Name the blood parasite species.
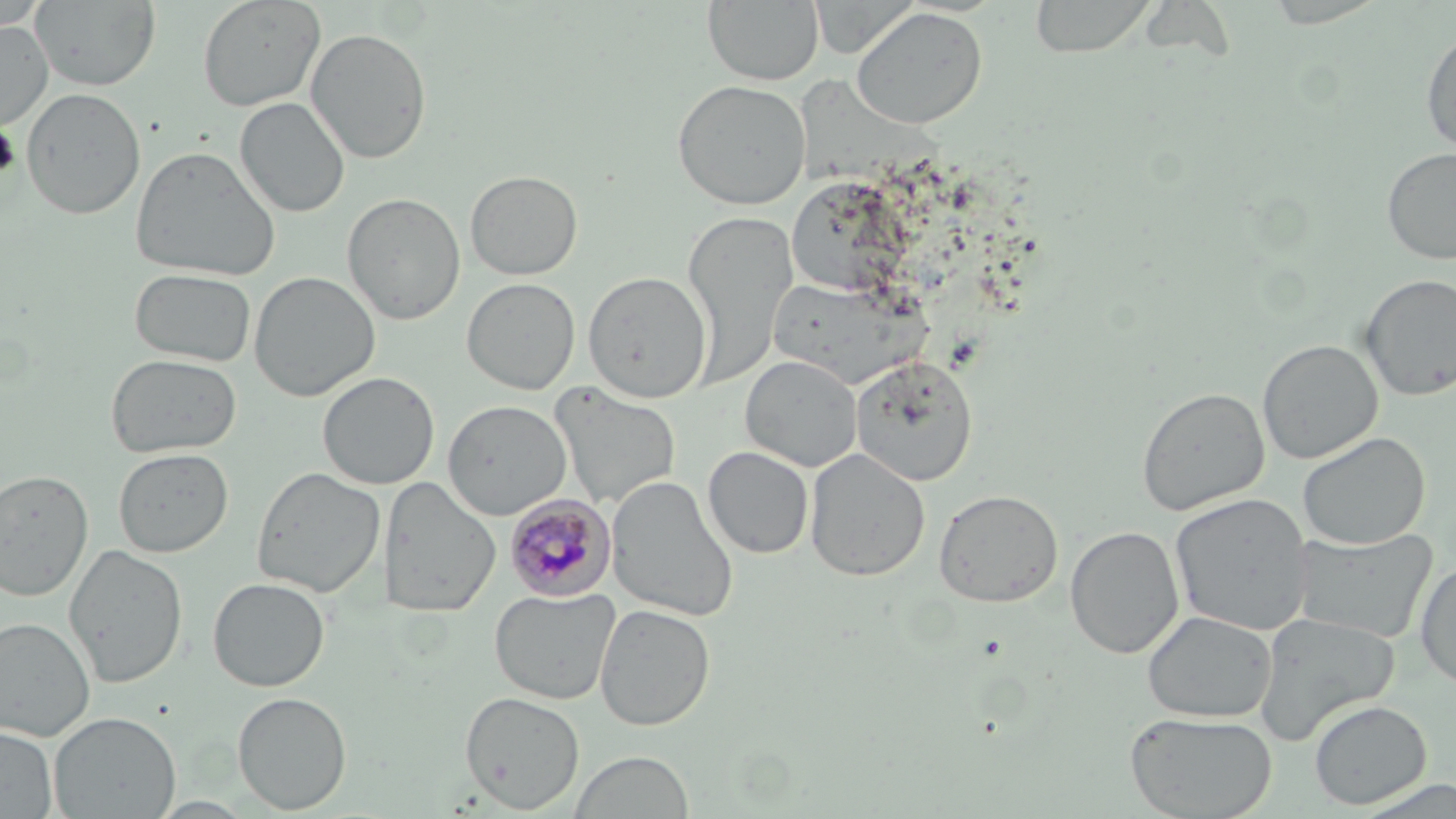
Plasmodium malariae.

Approximate bounding boxes as named x1/y1/x2/y2 corners in pixels. Platelet locations: (x1=0, y1=124, x2=20, y2=181). Uninfected red blood cell locations: (x1=31, y1=0, x2=161, y2=91), (x1=196, y1=0, x2=326, y2=112), (x1=702, y1=0, x2=824, y2=86), (x1=1028, y1=0, x2=1158, y2=58), (x1=0, y1=5, x2=47, y2=36), (x1=851, y1=6, x2=988, y2=129), (x1=0, y1=20, x2=53, y2=131), (x1=1421, y1=25, x2=1456, y2=155), (x1=305, y1=27, x2=432, y2=164), (x1=671, y1=79, x2=811, y2=210), (x1=21, y1=87, x2=146, y2=219), (x1=235, y1=96, x2=350, y2=218), (x1=129, y1=145, x2=280, y2=281), (x1=1381, y1=147, x2=1456, y2=265), (x1=465, y1=170, x2=583, y2=280), (x1=341, y1=192, x2=465, y2=325), (x1=682, y1=212, x2=798, y2=385), (x1=129, y1=268, x2=257, y2=367), (x1=248, y1=270, x2=380, y2=401), (x1=582, y1=271, x2=712, y2=403), (x1=1359, y1=274, x2=1455, y2=401), (x1=462, y1=277, x2=580, y2=395), (x1=1257, y1=339, x2=1383, y2=464), (x1=106, y1=353, x2=242, y2=458), (x1=740, y1=355, x2=863, y2=472), (x1=851, y1=355, x2=978, y2=485), (x1=317, y1=372, x2=440, y2=490), (x1=550, y1=383, x2=681, y2=512), (x1=1136, y1=387, x2=1270, y2=516), (x1=442, y1=400, x2=572, y2=520), (x1=1297, y1=431, x2=1431, y2=550), (x1=703, y1=446, x2=814, y2=559), (x1=113, y1=448, x2=234, y2=558), (x1=804, y1=448, x2=930, y2=581), (x1=251, y1=466, x2=386, y2=599), (x1=0, y1=468, x2=94, y2=601), (x1=605, y1=475, x2=740, y2=622), (x1=379, y1=476, x2=502, y2=617), (x1=934, y1=489, x2=1063, y2=607), (x1=1169, y1=493, x2=1315, y2=636), (x1=1065, y1=526, x2=1184, y2=659), (x1=1292, y1=528, x2=1438, y2=643), (x1=64, y1=544, x2=188, y2=688), (x1=1414, y1=560, x2=1456, y2=688), (x1=207, y1=576, x2=330, y2=691), (x1=489, y1=587, x2=621, y2=705), (x1=594, y1=603, x2=716, y2=731), (x1=1143, y1=611, x2=1277, y2=723), (x1=1254, y1=612, x2=1400, y2=744), (x1=0, y1=617, x2=96, y2=741), (x1=232, y1=691, x2=352, y2=814), (x1=460, y1=691, x2=585, y2=813), (x1=1308, y1=699, x2=1432, y2=809), (x1=48, y1=711, x2=181, y2=818), (x1=1125, y1=711, x2=1278, y2=819), (x1=0, y1=725, x2=58, y2=818), (x1=569, y1=750, x2=696, y2=819). Plasmodium malariae-infected red blood cell locations: (x1=504, y1=495, x2=616, y2=601). May-Grünwald-Giemsa stain. One field of a larger specimen. Optical microscopy. Thin blood smear. 1000x magnification. Image is 1456×819 pixels.